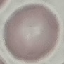
Result: negative for malaria parasites. Photographed with a smartphone camera at the microscope eyepiece. Giemsa stain. Cell patch, automatically extracted from a larger field of view and resized to 64 × 64 pixels. Thin blood smear.